Classify this cell by malaria status.
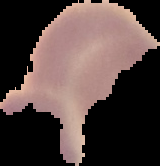

Uninfected.

Image is 160×166 pixels. From a thin blood film. The area outside the segmented cell region is set to black.